State which parasite is depicted.
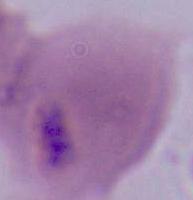

This is Plasmodium.

modality = photomicrograph
magnification = 400x or 1000x